Give the extent of all uninfected red blood cells.
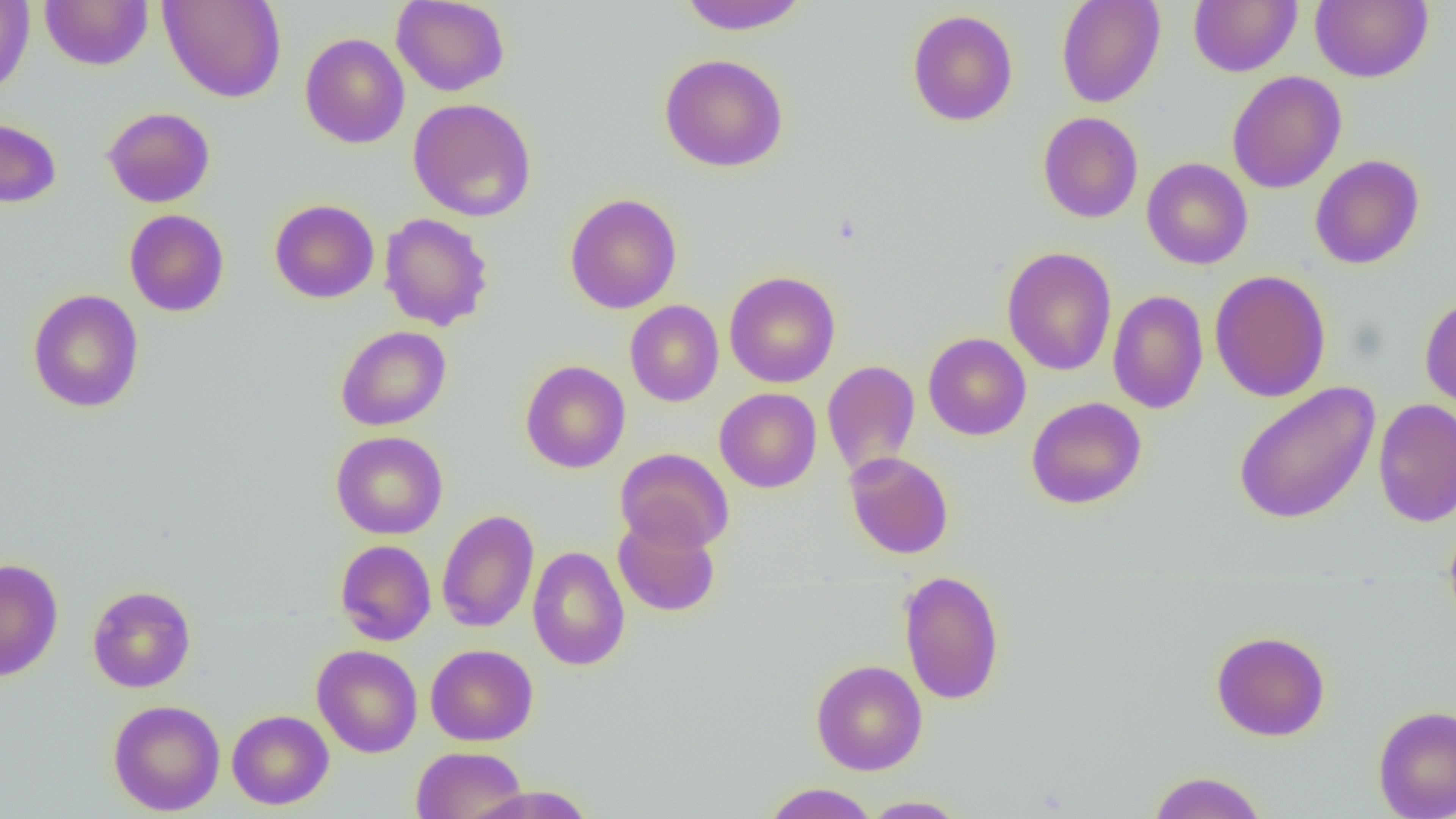

Approximate bounding boxes as [x1, y1, x2, y2] in pixels.
Uninfected red blood cells: [0, 0, 35, 97], [39, 0, 153, 70], [158, 0, 287, 103], [677, 0, 810, 35], [1055, 0, 1165, 108], [1189, 0, 1301, 77], [1311, 0, 1432, 83], [392, 1, 510, 97], [907, 9, 1018, 126], [299, 33, 410, 149], [659, 53, 789, 172], [1227, 70, 1347, 194], [408, 97, 537, 222], [102, 107, 215, 208], [1038, 111, 1143, 223], [0, 115, 62, 209], [1310, 154, 1425, 270], [1142, 158, 1253, 269], [564, 193, 682, 314], [269, 199, 379, 303], [124, 209, 229, 317], [378, 213, 494, 331], [1002, 247, 1117, 375], [1209, 269, 1331, 403], [724, 270, 840, 388], [28, 289, 144, 413], [1107, 289, 1208, 414], [1420, 295, 1456, 412], [625, 300, 724, 407], [335, 325, 451, 431], [923, 332, 1031, 440], [520, 360, 630, 474], [822, 360, 921, 480], [1232, 382, 1380, 524], [714, 387, 822, 493], [1026, 396, 1147, 509], [1374, 398, 1456, 528], [331, 430, 448, 539], [615, 447, 734, 553], [843, 451, 954, 559], [436, 509, 539, 633], [613, 513, 721, 618], [1444, 516, 1456, 632], [334, 539, 436, 646], [528, 545, 630, 671], [0, 558, 64, 682], [898, 569, 1006, 705], [87, 585, 196, 692], [1211, 630, 1330, 741], [311, 644, 423, 757], [426, 644, 538, 746], [811, 660, 927, 775], [108, 699, 225, 816], [1373, 704, 1456, 819], [227, 709, 334, 810], [410, 746, 528, 819], [1147, 770, 1268, 819], [762, 783, 879, 818], [465, 784, 599, 819], [859, 795, 971, 818].

slide-level diagnosis = no evidence of blood parasites
modality = light microscopy
preparation = thin blood smear
magnification = 1000x
image size = 1456×819 pixels
field of view = one of a larger specimen